Report the malaria status of this cell.
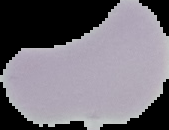
It is uninfected.

preparation = thin blood smear
image type = cell region segmented out of the field of view; surrounding area masked to black
image size = 169×130 pixels